Assess the morphology of the erythrocytes.
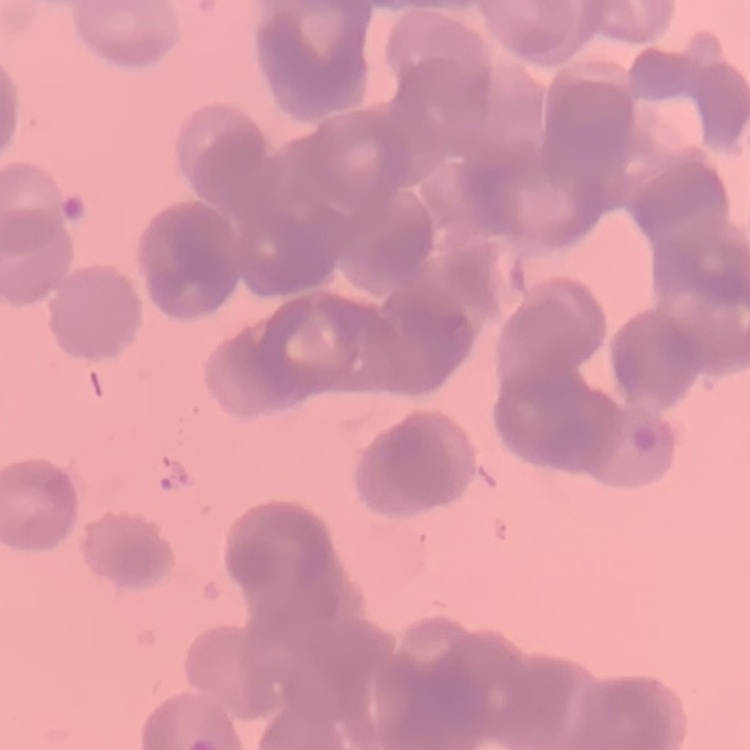
Rouleaux formation.

Thin peripheral smear. One tile cut from a larger photomicrograph. Field's or Giemsa stain.